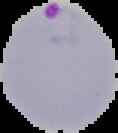
Summary:
  - Image type: cell region segmented out of the field of view; surrounding area masked to black
  - Malaria status: parasitized
  - Image size: 118×133 pixels
  - Preparation: thin blood film